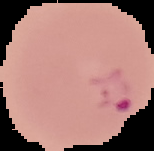

Summary:
  - Image type: segmented cell region on a black background
  - Preparation: thin blood smear
  - Result: malaria parasites detected
  - Image size: 154×151 pixels